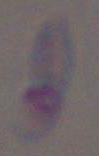
Toxoplasma gondii is seen. 1000x magnification. Photomicrograph.